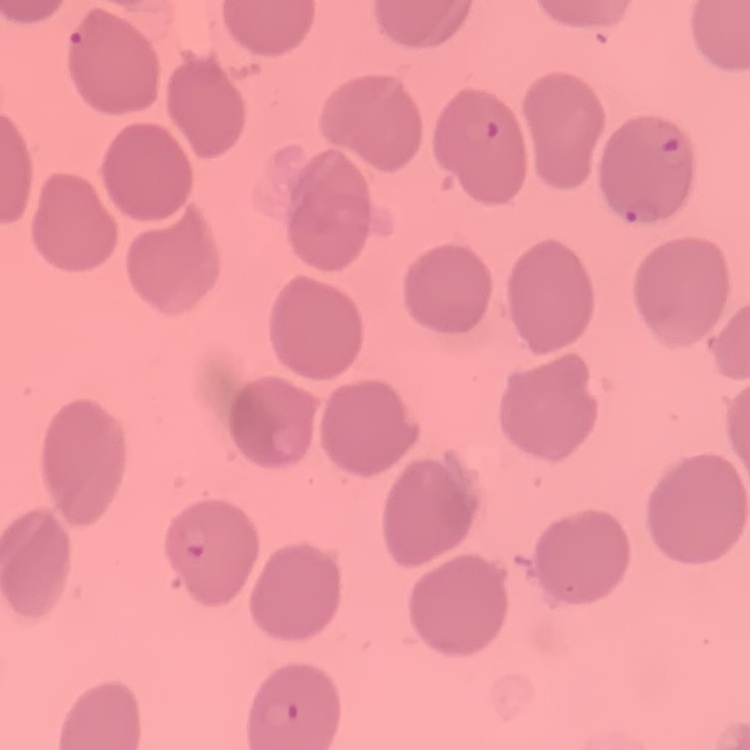
erythrocyte_morphology: no rouleaux formation
preparation: thin blood film
image_type: one tile cut from a larger photomicrograph
stain: Field's or Giemsa